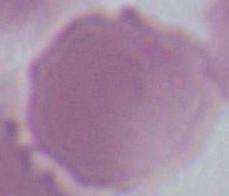

Summary:
  - Modality: micrograph
  - Magnification: 1000x
  - Identification: red blood cell